Locate every blood parasite and identify its species.
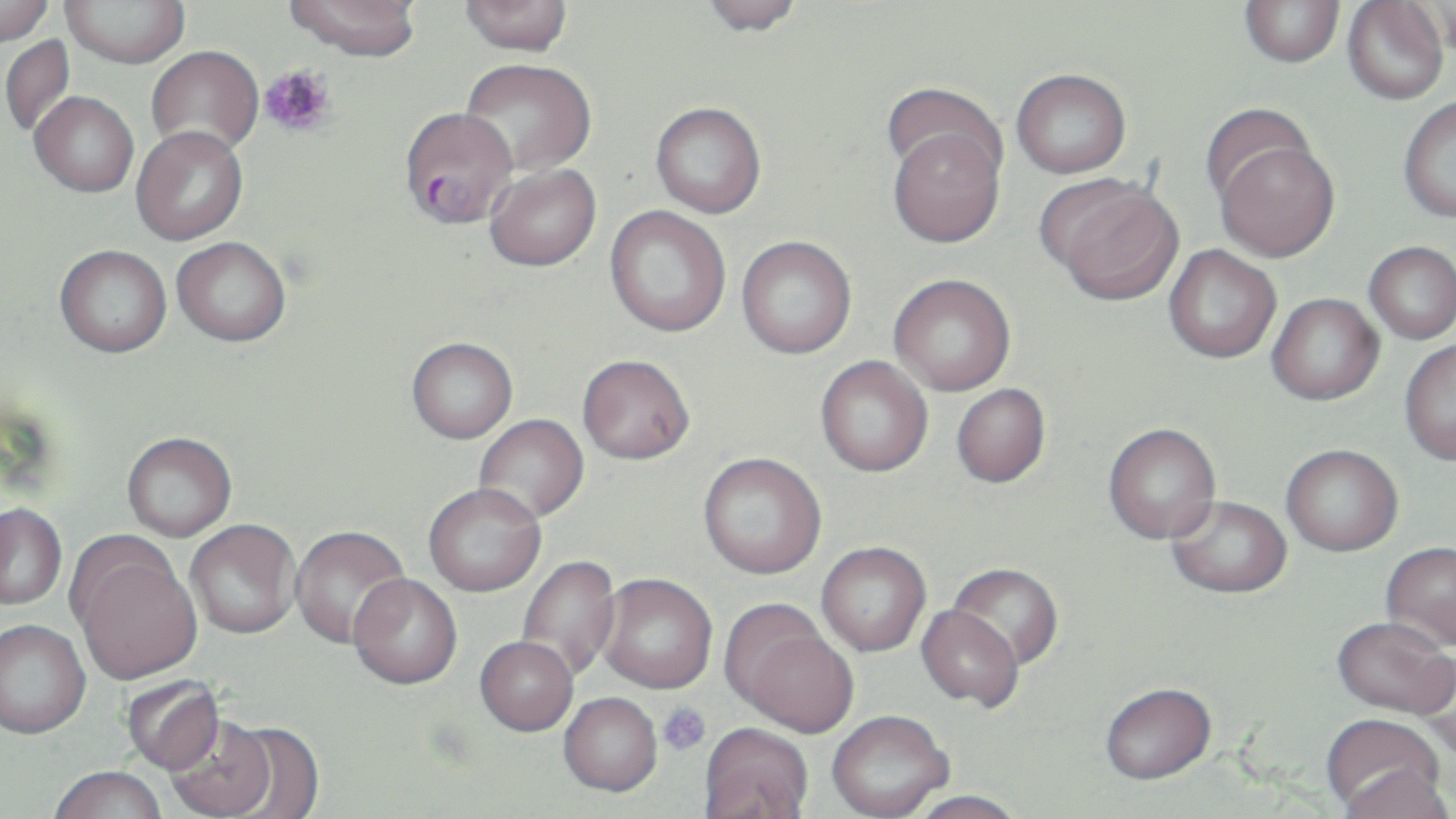
Approximate bounding boxes as [x1, y1, x2, y2] in pixels.
Plasmodium falciparum-infected red blood cells: [399, 106, 517, 228].
No Plasmodium ovale, Plasmodium malariae, Plasmodium vivax, Babesia divergens, or Trypanosoma brucei observed.

Uninfected red blood cell locations: [0, 0, 54, 46], [61, 0, 189, 67], [284, 0, 422, 60], [460, 0, 573, 55], [698, 0, 806, 36], [1434, 0, 1456, 61], [1240, 1, 1344, 67], [1343, 1, 1449, 105], [1, 35, 76, 137], [146, 46, 263, 158], [460, 58, 596, 176], [1011, 68, 1131, 178], [881, 83, 1004, 183], [30, 91, 139, 196], [1398, 96, 1456, 222], [651, 102, 766, 218], [1199, 103, 1317, 208], [886, 123, 1006, 247], [131, 125, 248, 245], [1215, 141, 1339, 261], [484, 163, 601, 271], [1046, 180, 1183, 305], [605, 206, 731, 337], [736, 235, 857, 358], [172, 237, 291, 346], [1364, 241, 1456, 344], [55, 245, 171, 357], [1163, 246, 1281, 363], [889, 274, 1016, 396], [1267, 293, 1384, 405], [407, 337, 518, 444], [1399, 339, 1456, 465], [577, 354, 695, 464], [815, 356, 932, 477], [951, 384, 1050, 487], [474, 414, 589, 524], [1103, 423, 1220, 543], [121, 432, 237, 542], [1281, 444, 1403, 556], [698, 452, 826, 578], [423, 484, 546, 597], [1166, 495, 1291, 598], [0, 504, 66, 610], [185, 520, 301, 640], [290, 526, 411, 650], [69, 540, 202, 686], [816, 542, 931, 657], [1380, 543, 1456, 652], [517, 555, 621, 681], [948, 562, 1062, 670], [597, 574, 716, 694], [348, 575, 462, 692], [916, 604, 1023, 711], [726, 610, 858, 738], [1331, 617, 1455, 719], [0, 622, 91, 743], [475, 638, 577, 738], [1414, 655, 1456, 764], [121, 675, 226, 776], [1100, 684, 1216, 788], [559, 694, 662, 799], [827, 714, 953, 819], [1320, 714, 1447, 813], [166, 718, 277, 818], [221, 723, 324, 818], [698, 725, 814, 819], [1336, 766, 1453, 819], [48, 769, 167, 819], [907, 792, 1027, 819]. Platelet locations: [258, 64, 337, 138], [658, 702, 711, 755]. Slide-level diagnosis: Plasmodium falciparum. Single field of view. Thin blood film. May-Grünwald-Giemsa stain. Captured at 1000x magnification. Optical microscopy. Image is 1456×819 pixels.